Outline each uninfected red blood cell.
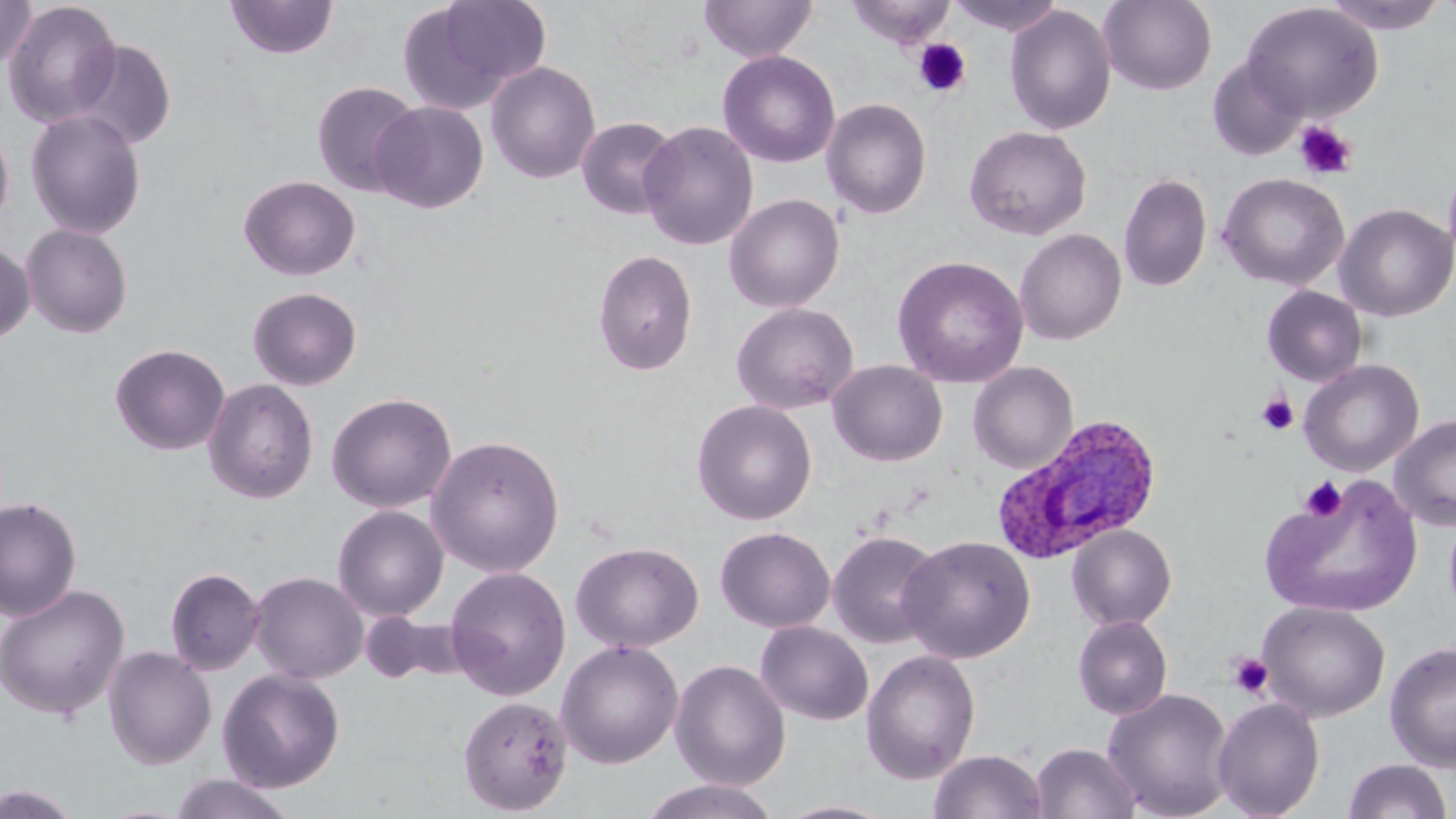
Approximate bounding boxes as named x1/y1/x2/y2 corners in pixels.
Uninfected red blood cells: (x1=0, y1=0, x2=36, y2=72), (x1=225, y1=0, x2=339, y2=60), (x1=399, y1=0, x2=548, y2=113), (x1=699, y1=0, x2=816, y2=62), (x1=847, y1=0, x2=955, y2=50), (x1=945, y1=0, x2=1067, y2=36), (x1=1098, y1=0, x2=1217, y2=95), (x1=1320, y1=0, x2=1450, y2=35), (x1=3, y1=1, x2=122, y2=128), (x1=1242, y1=3, x2=1383, y2=122), (x1=1005, y1=5, x2=1117, y2=136), (x1=69, y1=39, x2=177, y2=151), (x1=717, y1=50, x2=840, y2=168), (x1=1207, y1=58, x2=1307, y2=161), (x1=485, y1=61, x2=601, y2=184), (x1=311, y1=81, x2=423, y2=197), (x1=821, y1=98, x2=932, y2=219), (x1=370, y1=100, x2=489, y2=214), (x1=24, y1=109, x2=147, y2=240), (x1=576, y1=116, x2=681, y2=219), (x1=0, y1=119, x2=14, y2=229), (x1=639, y1=120, x2=758, y2=251), (x1=964, y1=125, x2=1092, y2=241), (x1=1443, y1=161, x2=1456, y2=273), (x1=1118, y1=172, x2=1212, y2=292), (x1=1217, y1=172, x2=1350, y2=291), (x1=238, y1=175, x2=361, y2=281), (x1=724, y1=193, x2=845, y2=313), (x1=1335, y1=203, x2=1456, y2=322), (x1=21, y1=223, x2=133, y2=338), (x1=1014, y1=228, x2=1126, y2=345), (x1=0, y1=242, x2=35, y2=345), (x1=593, y1=249, x2=698, y2=376), (x1=892, y1=255, x2=1029, y2=388), (x1=1261, y1=285, x2=1367, y2=387), (x1=247, y1=286, x2=362, y2=391), (x1=731, y1=301, x2=859, y2=415), (x1=110, y1=343, x2=230, y2=455), (x1=1298, y1=359, x2=1424, y2=477), (x1=828, y1=360, x2=947, y2=467), (x1=968, y1=361, x2=1078, y2=474), (x1=203, y1=378, x2=318, y2=505), (x1=326, y1=392, x2=457, y2=513), (x1=692, y1=399, x2=817, y2=525), (x1=1390, y1=413, x2=1456, y2=531), (x1=426, y1=434, x2=565, y2=577), (x1=1261, y1=472, x2=1424, y2=620), (x1=0, y1=496, x2=82, y2=622), (x1=332, y1=505, x2=449, y2=621), (x1=1067, y1=524, x2=1177, y2=630), (x1=715, y1=526, x2=836, y2=633), (x1=827, y1=530, x2=944, y2=649), (x1=898, y1=534, x2=1036, y2=664), (x1=571, y1=541, x2=704, y2=653), (x1=444, y1=566, x2=571, y2=701), (x1=165, y1=567, x2=265, y2=676), (x1=249, y1=572, x2=368, y2=684), (x1=0, y1=584, x2=129, y2=719), (x1=1258, y1=601, x2=1391, y2=722), (x1=360, y1=611, x2=461, y2=686), (x1=1072, y1=615, x2=1173, y2=720), (x1=755, y1=621, x2=873, y2=726), (x1=556, y1=639, x2=684, y2=768), (x1=1384, y1=641, x2=1456, y2=772), (x1=104, y1=646, x2=216, y2=769), (x1=861, y1=649, x2=981, y2=784), (x1=670, y1=659, x2=791, y2=791), (x1=217, y1=668, x2=345, y2=792), (x1=1102, y1=688, x2=1236, y2=819), (x1=457, y1=695, x2=573, y2=815), (x1=1212, y1=697, x2=1326, y2=818), (x1=1032, y1=742, x2=1141, y2=819), (x1=928, y1=749, x2=1048, y2=819), (x1=1342, y1=758, x2=1453, y2=818), (x1=168, y1=773, x2=298, y2=819), (x1=638, y1=778, x2=783, y2=819), (x1=0, y1=785, x2=82, y2=819), (x1=771, y1=800, x2=899, y2=819).

Plasmodium ovale-infected red blood cell locations: (x1=991, y1=413, x2=1163, y2=565). Platelet locations: (x1=913, y1=38, x2=972, y2=98), (x1=1294, y1=120, x2=1358, y2=180), (x1=1257, y1=393, x2=1299, y2=436), (x1=1299, y1=476, x2=1347, y2=522), (x1=1227, y1=653, x2=1273, y2=699). Slide-level diagnosis: Plasmodium ovale. One field of a larger specimen. Captured at 1000x magnification. May-Grünwald-Giemsa-stained preparation. Image is 1456×819 pixels. Optical microscopy. Thin blood smear.